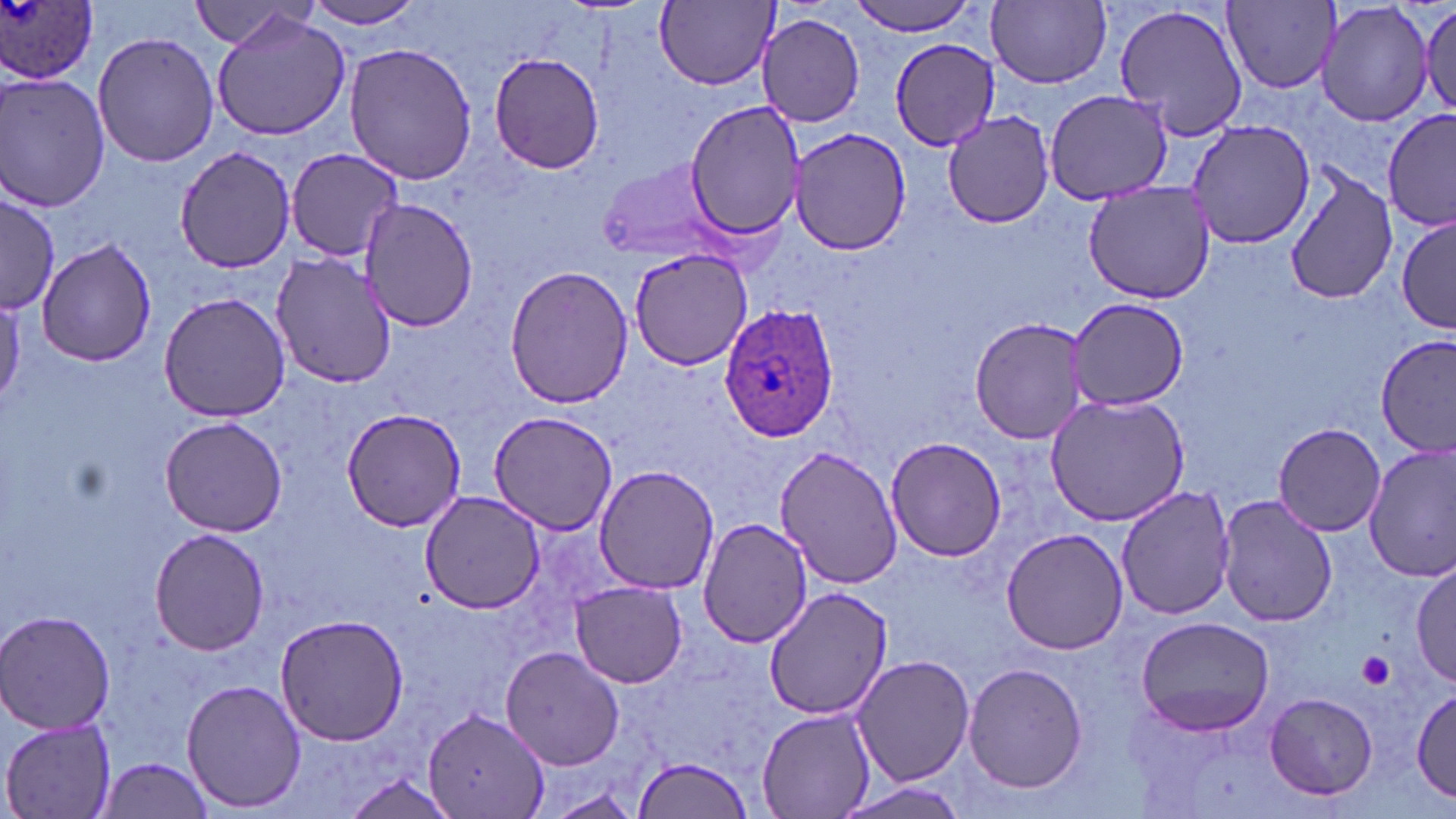
slide-level diagnosis = Plasmodium ovale
uninfected red blood cell locations = approximate bounding boxes as (x1,y1)-(x2,y2) corner pairs in pixels: (300,0)-(430,29), (846,0)-(987,36), (1225,0)-(1339,91), (1316,0)-(1434,129), (655,1)-(777,89), (987,1)-(1111,88), (187,2)-(305,49), (1416,2)-(1455,119), (1114,3)-(1249,142), (209,8)-(355,141), (757,12)-(867,126), (91,32)-(220,169), (890,38)-(1002,151), (343,42)-(480,184), (488,52)-(606,174), (0,71)-(111,214), (1044,88)-(1173,204), (684,98)-(806,242), (1383,107)-(1455,234), (940,108)-(1057,226), (1186,119)-(1317,249), (789,128)-(912,254), (171,144)-(298,271), (286,147)-(407,262), (597,156)-(729,266), (1284,166)-(1398,306), (1082,180)-(1215,305), (1,192)-(60,312), (360,198)-(478,332), (1396,212)-(1454,335), (37,236)-(157,368), (628,247)-(752,370), (270,252)-(399,389), (503,265)-(633,411), (157,293)-(293,423), (1069,297)-(1189,408), (970,314)-(1094,445), (1376,335)-(1454,459), (1043,392)-(1192,526), (341,408)-(468,533), (488,410)-(622,536), (161,416)-(289,535), (1272,423)-(1387,536), (885,435)-(1007,561), (1364,444)-(1456,584), (777,446)-(904,589), (593,466)-(721,594), (1116,487)-(1236,622), (420,490)-(547,613), (1216,496)-(1338,628), (697,517)-(813,648), (1000,527)-(1130,655), (150,528)-(270,657), (1412,561)-(1455,687), (570,582)-(689,689), (763,586)-(891,720), (1,610)-(117,735), (272,612)-(409,744), (1135,616)-(1275,735), (500,645)-(626,771), (852,654)-(975,785), (963,663)-(1088,793), (182,678)-(307,813), (1412,688)-(1455,802), (1265,692)-(1380,801), (426,706)-(549,816), (757,708)-(876,818), (1,716)-(118,819), (630,754)-(755,819), (99,757)-(216,817), (340,771)-(459,818), (832,780)-(972,818)
modality = light microscopy
preparation = thin blood film
magnification = 1000x
image size = 1456×819 pixels
platelet locations = approximate bounding boxes as (x1,y1)-(x2,y2) corner pairs in pixels: (1358,652)-(1394,689)
stain = May-Grünwald-Giemsa
Plasmodium ovale-infected red blood cell locations = approximate bounding boxes as (x1,y1)-(x2,y2) corner pairs in pixels: (0,0)-(103,88), (722,307)-(840,441)
field of view = single